Assess the morphology of the red blood cells.
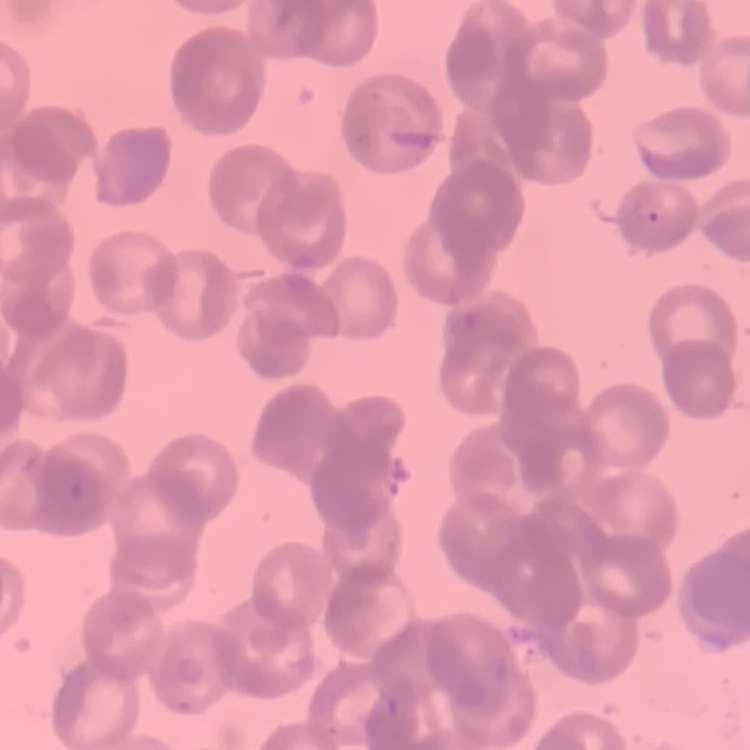

They show rouleaux formation.

image type = one tile cut from a larger photomicrograph
preparation = thin peripheral smear
stain = Field's or Giemsa